Report the malaria status of this cell.
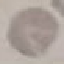

Uninfected.

Cell patch, automatically extracted from a larger field of view and resized to 64 × 64 pixels. Photographed with a smartphone camera at the microscope eyepiece. Thin blood film. Giemsa stain.